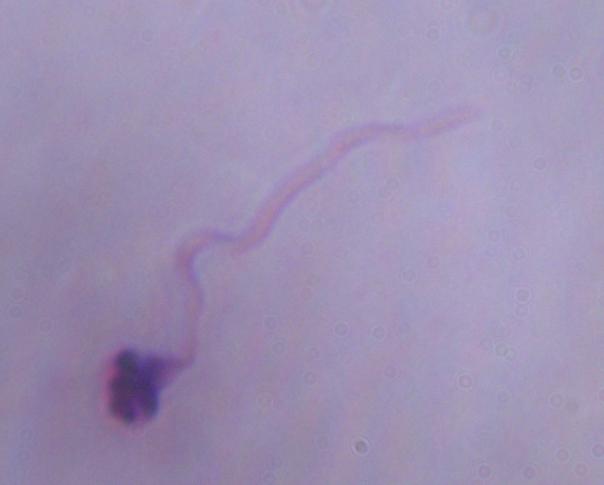
Summary:
  - Identification: Leishmania
  - Modality: micrograph
  - Magnification: 1000x